Assess the morphology of the red blood cells.
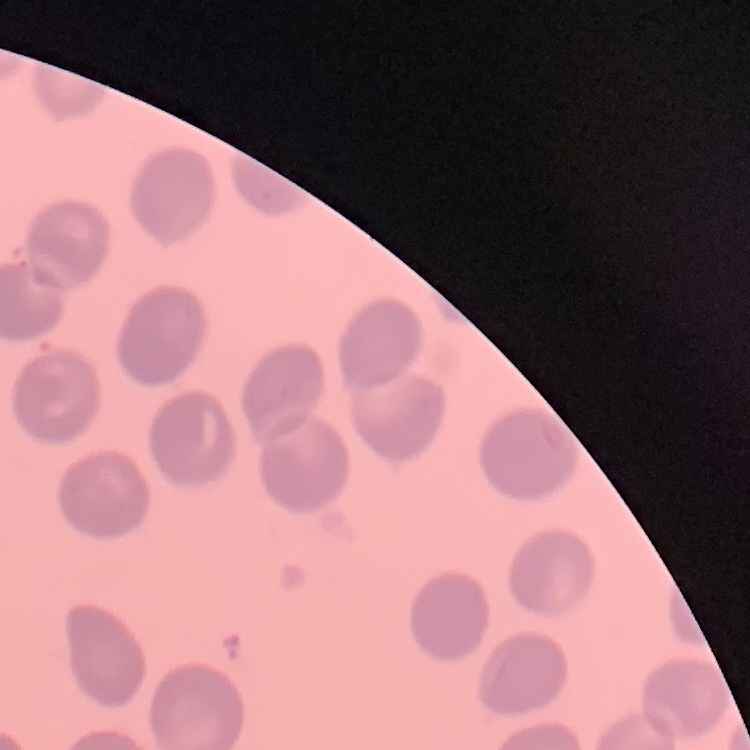
No rouleaux formation.

Summary:
  - Image type: square crop of a larger photomicrograph
  - Stain: Field's or Giemsa
  - Preparation: thin peripheral smear